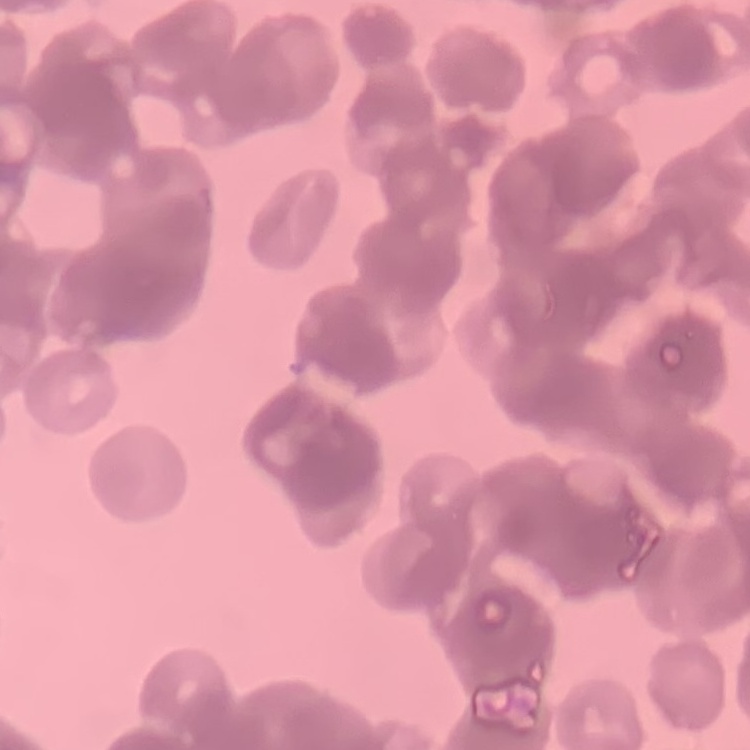

Summary:
  - Erythrocyte morphology: rouleaux formation
  - Image type: square crop of a larger photomicrograph
  - Preparation: thin peripheral smear
  - Stain: Field's or Giemsa